Identify the blood parasite species.
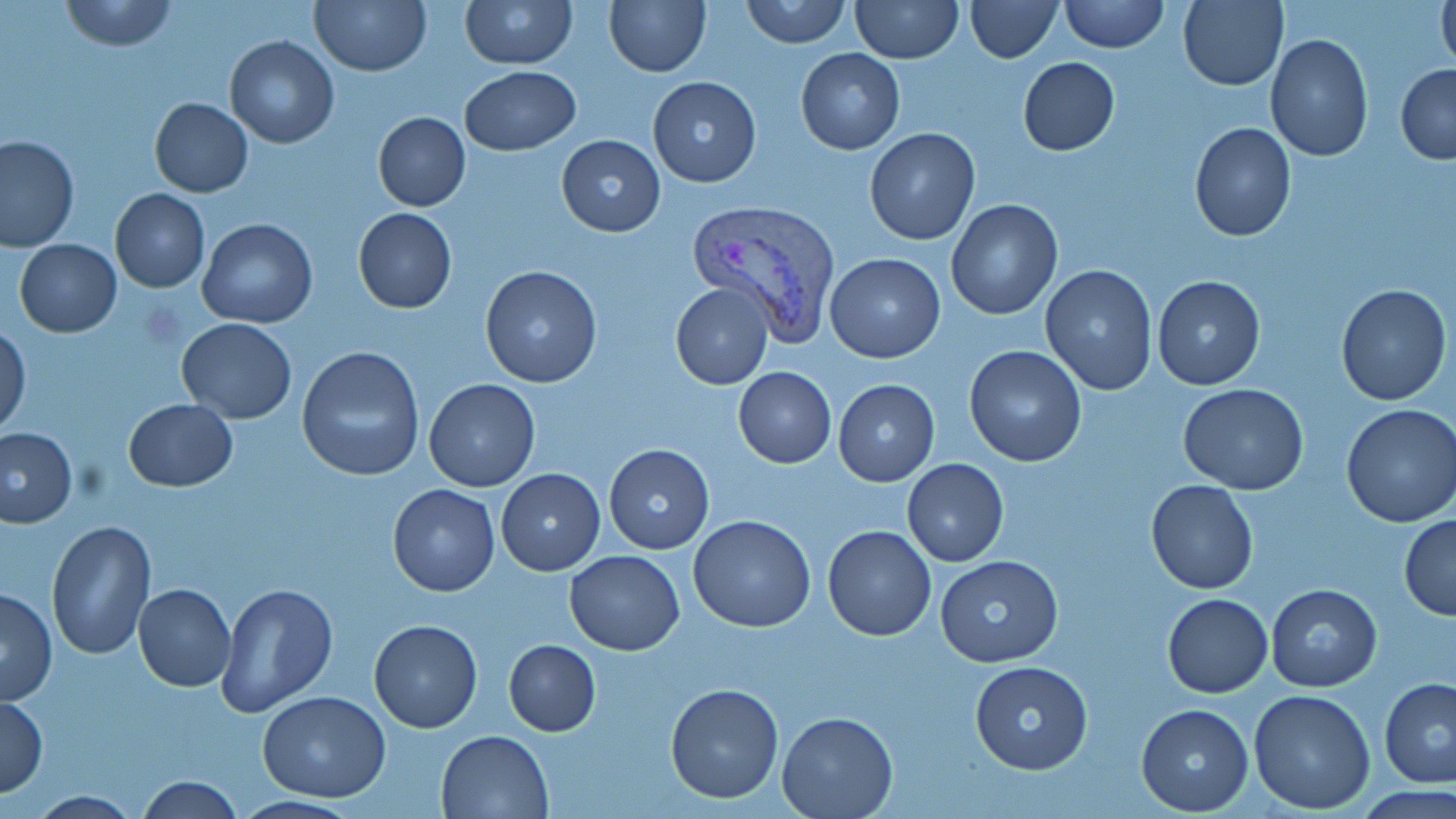

Plasmodium vivax.

Approximate bounding boxes as [x1, y1, x2, y2] in pixels. Uninfected red blood cell locations: [60, 0, 178, 52], [310, 0, 432, 77], [460, 0, 578, 70], [604, 0, 711, 77], [739, 0, 852, 47], [849, 0, 963, 64], [963, 0, 1063, 63], [1059, 0, 1167, 53], [1177, 0, 1288, 91], [1436, 0, 1456, 74], [1265, 34, 1373, 160], [225, 35, 339, 148], [796, 49, 904, 154], [1017, 57, 1121, 156], [1396, 64, 1456, 164], [459, 65, 580, 156], [647, 74, 762, 187], [149, 98, 253, 196], [373, 112, 471, 211], [1190, 122, 1297, 242], [864, 128, 979, 245], [555, 135, 665, 237], [0, 136, 80, 253], [110, 188, 210, 293], [945, 200, 1062, 320], [353, 208, 458, 313], [197, 218, 318, 328], [15, 240, 121, 337], [824, 252, 946, 364], [1040, 265, 1158, 395], [479, 266, 603, 388], [1152, 275, 1265, 390], [669, 281, 775, 390], [1335, 284, 1451, 405], [175, 318, 297, 424], [0, 327, 30, 436], [964, 345, 1087, 465], [296, 346, 424, 481], [732, 367, 836, 467], [423, 378, 540, 492], [833, 379, 940, 486], [1178, 382, 1309, 494], [124, 399, 238, 491], [1340, 402, 1456, 528], [1, 428, 77, 527], [603, 443, 714, 554], [902, 459, 1008, 566], [495, 469, 605, 576], [1146, 479, 1259, 594], [387, 485, 500, 596], [1399, 513, 1456, 620], [687, 514, 816, 633], [45, 519, 156, 658], [822, 524, 936, 641], [565, 550, 685, 656], [935, 554, 1063, 667], [216, 582, 337, 716], [1265, 582, 1382, 691], [134, 583, 236, 692], [0, 588, 57, 705], [1163, 593, 1273, 698], [369, 619, 483, 733], [503, 640, 601, 736], [969, 661, 1092, 774], [1378, 677, 1456, 789], [664, 682, 784, 803], [1248, 688, 1377, 814], [258, 692, 391, 802], [1, 696, 47, 795], [1136, 704, 1254, 815], [776, 712, 898, 819], [436, 729, 553, 817], [135, 776, 246, 817]. Plasmodium vivax-infected red blood cell locations: [686, 199, 842, 342]. Image is 1456×819 pixels. 1000x magnification. Light microscopy. May-Grünwald-Giemsa-stained preparation. Single field of view. Thin blood smear.